State the blood parasite species.
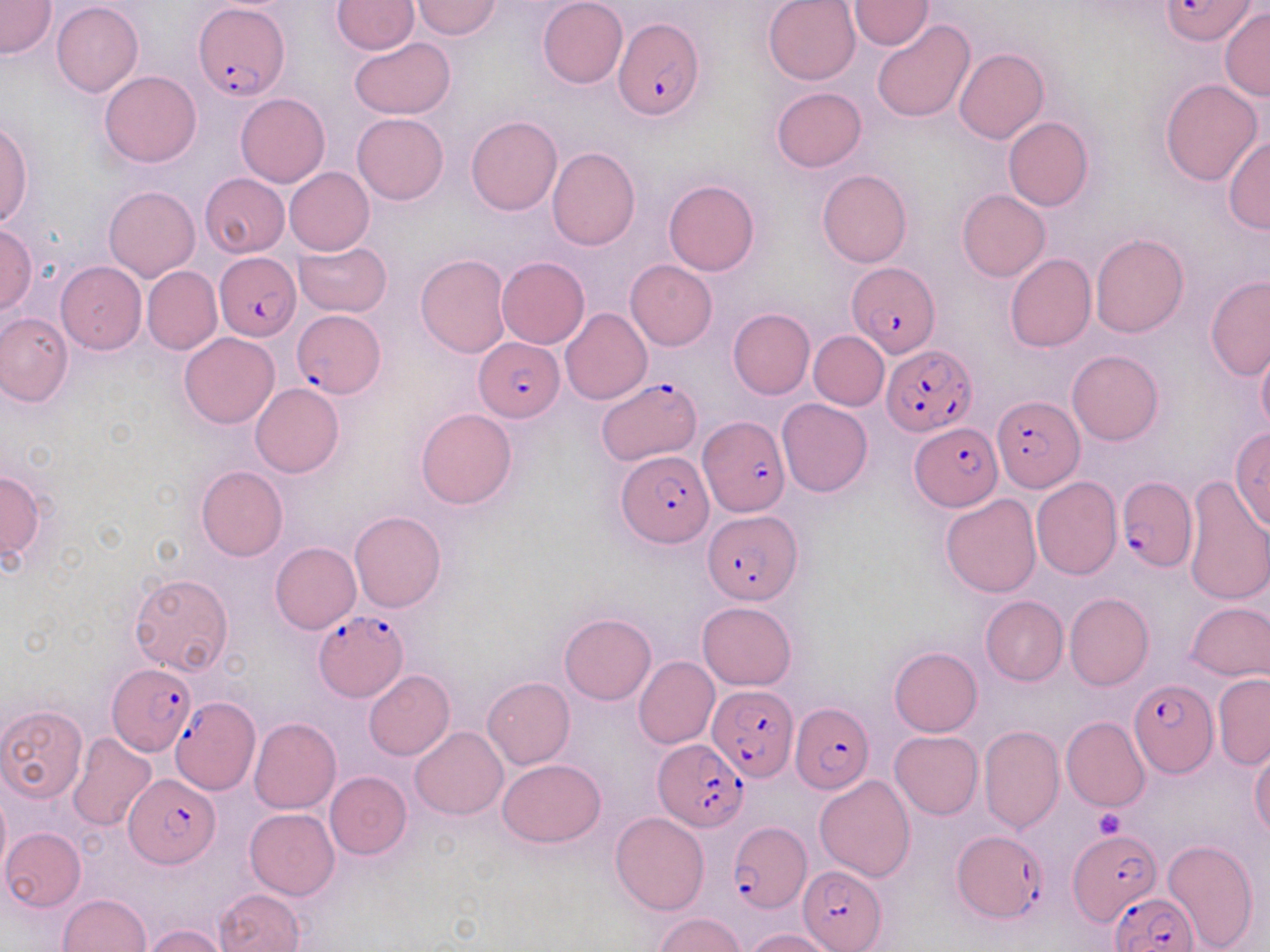

Plasmodium falciparum.

{
  "field_of_view": "one of a larger specimen",
  "preparation": "thin blood smear",
  "platelet_locations": "approximate bounding boxes as [x1, y1, x2, y2] in pixels: [1094, 808, 1124, 837]",
  "image_size": "1270×952 pixels",
  "magnification": "1000x",
  "stain": "May-Grünwald-Giemsa",
  "plasmodium_falciparum_infected_red_blood_cell_locations": "approximate bounding boxes as [x1, y1, x2, y2] in pixels: [1161, 0, 1256, 45], [195, 4, 288, 102], [614, 21, 705, 120], [215, 252, 302, 340], [846, 262, 939, 356], [292, 310, 385, 398], [473, 335, 564, 419], [881, 344, 976, 437], [597, 378, 702, 463], [992, 396, 1083, 493], [699, 417, 790, 516], [911, 423, 1002, 509], [617, 449, 712, 547], [1117, 478, 1195, 576], [702, 508, 801, 602], [313, 608, 407, 700], [108, 662, 196, 755], [1129, 679, 1219, 778], [708, 685, 799, 780], [170, 693, 261, 799], [790, 702, 873, 794], [654, 739, 746, 831], [126, 773, 217, 867], [728, 821, 810, 914], [952, 830, 1046, 926], [1069, 830, 1163, 926], [797, 866, 886, 950], [1108, 890, 1199, 952]",
  "modality": "light microscopy",
  "uninfected_red_blood_cell_locations": "approximate bounding boxes as [x1, y1, x2, y2] in pixels: [538, 0, 628, 89], [763, 0, 862, 86], [0, 1, 56, 59], [332, 1, 419, 53], [411, 1, 502, 39], [848, 1, 932, 50], [51, 2, 143, 97], [1218, 7, 1270, 103], [871, 20, 976, 123], [350, 37, 454, 118], [954, 47, 1048, 143], [99, 70, 201, 167], [1160, 78, 1262, 185], [771, 87, 868, 173], [236, 93, 330, 187], [352, 113, 448, 204], [466, 115, 562, 215], [1004, 117, 1093, 211], [0, 119, 32, 228], [1223, 136, 1270, 233], [546, 146, 640, 251], [284, 167, 374, 255], [816, 169, 912, 268], [199, 173, 289, 257], [664, 179, 759, 276], [104, 185, 200, 281], [957, 189, 1050, 281], [0, 223, 37, 316], [1090, 233, 1188, 338], [292, 240, 393, 317], [416, 253, 512, 358], [1004, 254, 1096, 352], [497, 256, 589, 349], [625, 261, 716, 350], [56, 262, 145, 354], [142, 266, 222, 354], [1205, 276, 1270, 381], [561, 307, 652, 405], [728, 308, 815, 399], [1, 311, 72, 407], [808, 331, 889, 410], [179, 332, 279, 428], [1256, 343, 1270, 439], [1067, 349, 1162, 445], [250, 383, 344, 477], [777, 398, 872, 497], [416, 408, 517, 509], [1230, 429, 1270, 530], [195, 465, 288, 561], [0, 470, 47, 562], [1183, 475, 1270, 606], [1032, 477, 1122, 579], [940, 494, 1042, 598], [349, 511, 447, 612], [270, 543, 360, 633], [130, 572, 234, 674], [1064, 592, 1155, 691], [980, 595, 1068, 685], [1186, 600, 1270, 682], [697, 601, 798, 690], [559, 614, 656, 705], [888, 647, 983, 737], [634, 656, 719, 750], [364, 670, 454, 760], [1213, 674, 1270, 768], [482, 677, 575, 769], [0, 705, 87, 803], [1061, 717, 1150, 813], [249, 718, 342, 814], [978, 725, 1063, 834], [409, 726, 506, 820], [890, 730, 983, 819], [68, 732, 158, 831], [1250, 746, 1270, 839], [497, 759, 604, 848], [325, 771, 412, 859], [815, 775, 916, 883], [0, 788, 10, 880], [244, 808, 339, 899], [611, 812, 709, 915], [1, 828, 86, 911], [1163, 839, 1260, 951], [215, 889, 304, 952], [58, 894, 151, 952], [656, 913, 743, 952], [141, 924, 229, 952], [744, 928, 835, 951]"
}